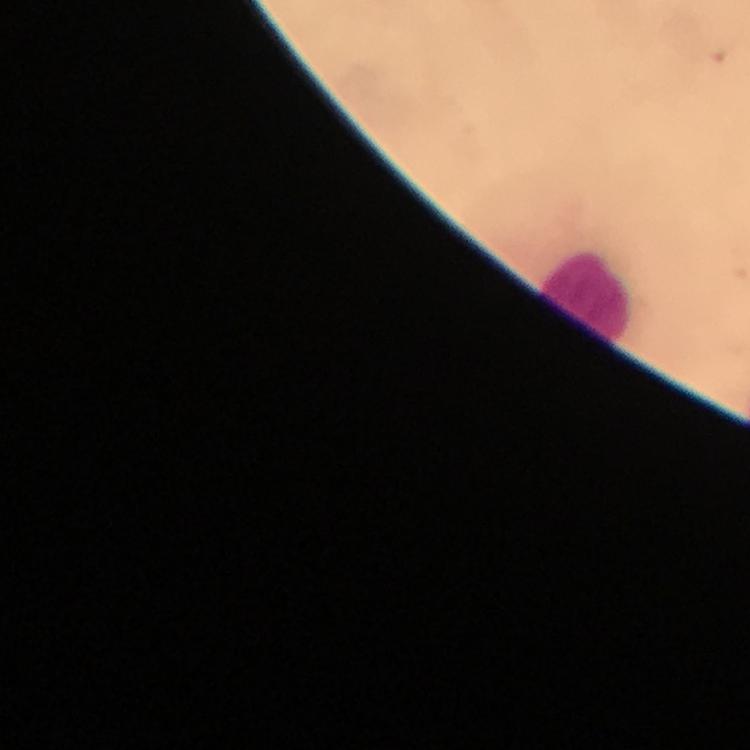

Approximate centers as (x, y) in pixels. Leukocyte locations: (587, 297). Giemsa stain. A crop from one field of view. 100x magnification. Image is 750×750 pixels. Immersion oil applied. Photographed with a smartphone mounted on the microscope. Thick blood film. Malaria parasites: none detected. From a diagnostic examination for malaria.